Outline platelets.
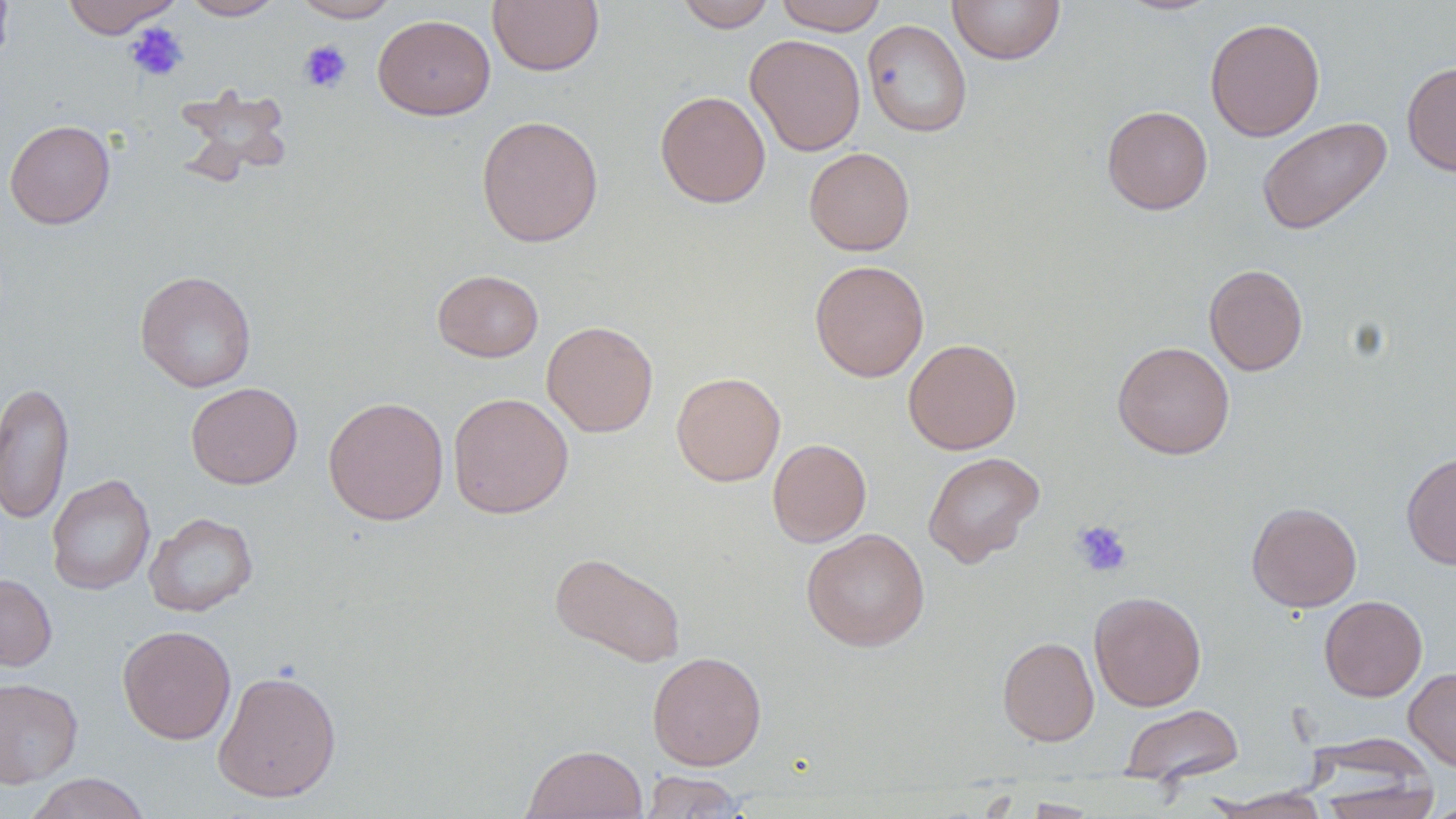
Approximate bounding boxes as named x1/y1/x2/y2 corners in pixels.
Platelets: (x1=124, y1=22, x2=188, y2=82), (x1=298, y1=40, x2=353, y2=93), (x1=1071, y1=520, x2=1132, y2=577).

slide_level_diagnosis: no evidence of blood parasites
modality: optical microscopy
stain: May-Grünwald-Giemsa
magnification: 1000x
image_size: 1456×819 pixels
uninfected_red_blood_cell_locations: 'approximate bounding boxes as named x1/y1/x2/y2 corners in pixels: (x1=0, y1=0, x2=14, y2=71), (x1=61, y1=0, x2=181, y2=38), (x1=182, y1=0, x2=284, y2=20), (x1=292, y1=0, x2=400, y2=22), (x1=487, y1=0, x2=604, y2=75), (x1=675, y1=0, x2=775, y2=32), (x1=774, y1=0, x2=887, y2=35), (x1=947, y1=0, x2=1066, y2=65), (x1=1115, y1=0, x2=1222, y2=16), (x1=373, y1=14, x2=495, y2=120), (x1=1205, y1=16, x2=1325, y2=142), (x1=862, y1=19, x2=972, y2=138), (x1=745, y1=34, x2=866, y2=156), (x1=1402, y1=61, x2=1456, y2=177), (x1=173, y1=84, x2=294, y2=186), (x1=655, y1=90, x2=771, y2=208), (x1=1101, y1=105, x2=1213, y2=215), (x1=476, y1=114, x2=604, y2=248), (x1=1257, y1=116, x2=1393, y2=235), (x1=4, y1=119, x2=116, y2=229), (x1=804, y1=147, x2=915, y2=255), (x1=809, y1=260, x2=929, y2=382), (x1=1204, y1=264, x2=1308, y2=375), (x1=135, y1=269, x2=257, y2=392), (x1=432, y1=269, x2=543, y2=362), (x1=541, y1=320, x2=658, y2=438), (x1=903, y1=338, x2=1021, y2=455), (x1=1113, y1=341, x2=1235, y2=459), (x1=671, y1=371, x2=785, y2=486), (x1=0, y1=380, x2=74, y2=524), (x1=185, y1=382, x2=303, y2=489), (x1=448, y1=392, x2=574, y2=519), (x1=322, y1=396, x2=449, y2=525), (x1=767, y1=438, x2=872, y2=547), (x1=923, y1=451, x2=1045, y2=567), (x1=1401, y1=451, x2=1456, y2=570), (x1=47, y1=474, x2=156, y2=595), (x1=1246, y1=502, x2=1362, y2=612), (x1=144, y1=511, x2=258, y2=617), (x1=801, y1=528, x2=930, y2=651), (x1=549, y1=551, x2=686, y2=668), (x1=0, y1=574, x2=57, y2=671), (x1=1089, y1=591, x2=1206, y2=711), (x1=1319, y1=595, x2=1427, y2=701), (x1=118, y1=624, x2=236, y2=744), (x1=997, y1=636, x2=1099, y2=746), (x1=647, y1=651, x2=767, y2=770), (x1=1404, y1=666, x2=1456, y2=772), (x1=213, y1=669, x2=342, y2=803), (x1=0, y1=678, x2=83, y2=788), (x1=1121, y1=704, x2=1244, y2=788), (x1=522, y1=744, x2=648, y2=819), (x1=639, y1=770, x2=748, y2=818), (x1=24, y1=772, x2=152, y2=819), (x1=1313, y1=774, x2=1441, y2=819), (x1=1210, y1=788, x2=1331, y2=818), (x1=1018, y1=798, x2=1101, y2=818), (x1=1425, y1=799, x2=1456, y2=818)'
field_of_view: one of a larger specimen
preparation: thin blood smear